Identify the parasite.
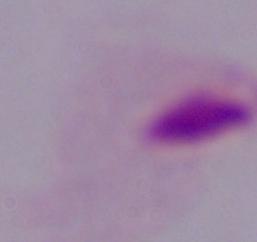
A trichomonad.

{
  "modality": "photomicrograph",
  "magnification": "1000x"
}